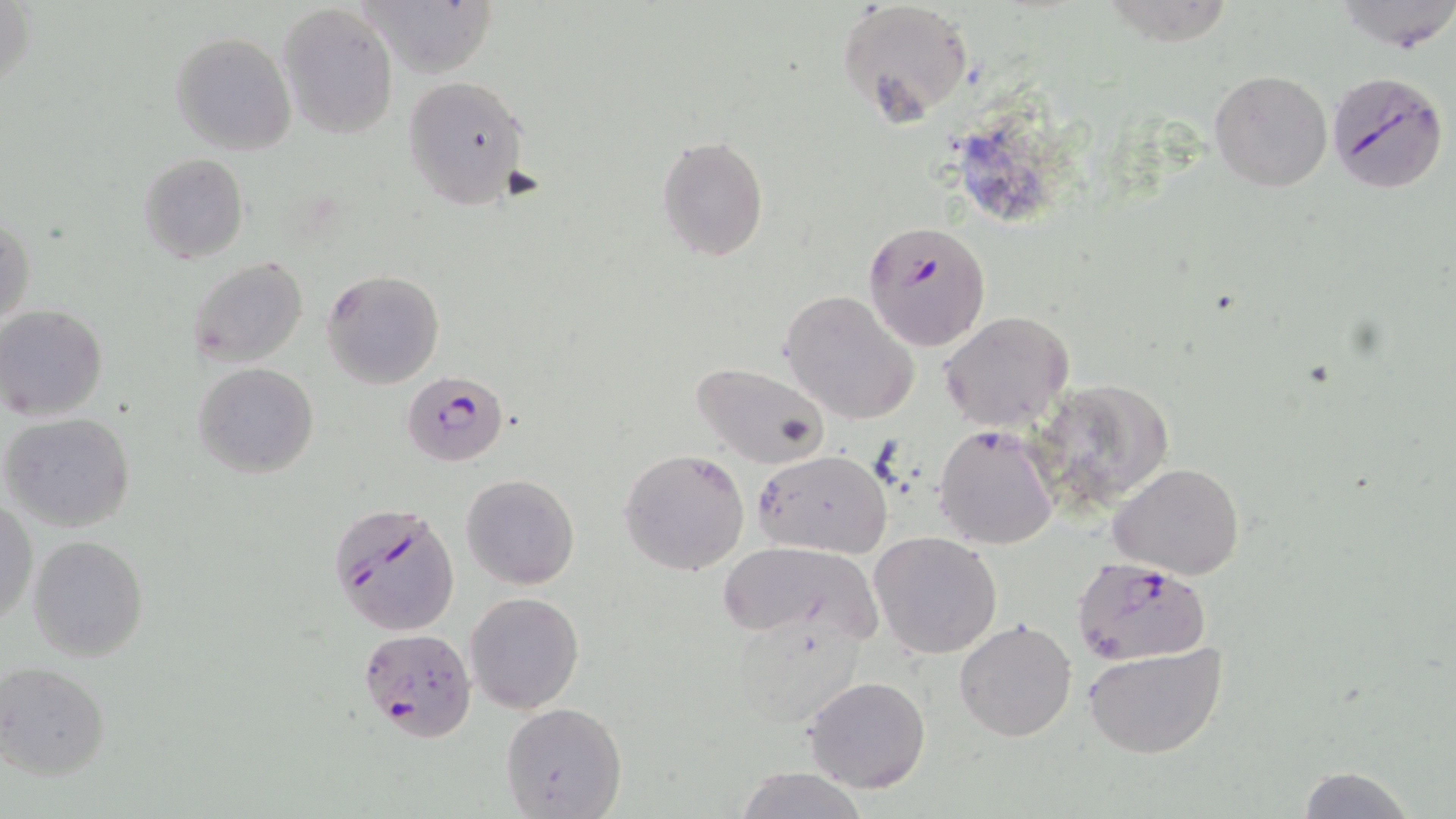
{
  "slide_level_diagnosis": "Plasmodium falciparum",
  "magnification": "1000x",
  "uninfected_red_blood_cell_locations": "approximate bounding boxes as [x1, y1, x2, y2] in pixels: [355, 0, 499, 78], [1334, 0, 1456, 53], [838, 1, 974, 124], [278, 3, 399, 137], [170, 31, 297, 156], [1208, 69, 1332, 193], [401, 74, 527, 211], [656, 135, 770, 261], [138, 153, 249, 264], [1, 214, 33, 332], [186, 255, 309, 368], [322, 271, 444, 389], [781, 290, 919, 425], [0, 305, 111, 422], [939, 311, 1074, 433], [692, 360, 829, 469], [194, 363, 319, 480], [1030, 376, 1176, 516], [1, 411, 136, 533], [934, 424, 1059, 551], [619, 448, 750, 577], [754, 450, 892, 559], [1108, 462, 1247, 581], [460, 474, 580, 589], [1, 499, 38, 626], [869, 532, 1002, 660], [27, 534, 149, 662], [717, 541, 882, 638], [465, 592, 583, 714], [730, 615, 868, 731], [953, 618, 1076, 742], [1082, 643, 1230, 760], [1, 661, 110, 781], [800, 675, 931, 792], [501, 700, 626, 817], [1294, 764, 1419, 819], [732, 766, 870, 819]",
  "modality": "optical microscopy",
  "field_of_view": "one of a larger specimen",
  "plasmodium_falciparum_infected_red_blood_cell_locations": "approximate bounding boxes as [x1, y1, x2, y2] in pixels: [1328, 70, 1450, 196], [861, 219, 992, 351], [402, 370, 509, 468], [326, 502, 461, 636], [1073, 556, 1210, 665], [358, 628, 475, 744]",
  "stain": "May-Grünwald-Giemsa",
  "image_size": "1456×819 pixels",
  "preparation": "thin blood film"
}